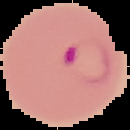

image_type: segmented cell region on a black background
result: Plasmodium parasites detected
preparation: thin blood smear
image_size: 130×130 pixels